State the blood parasite species.
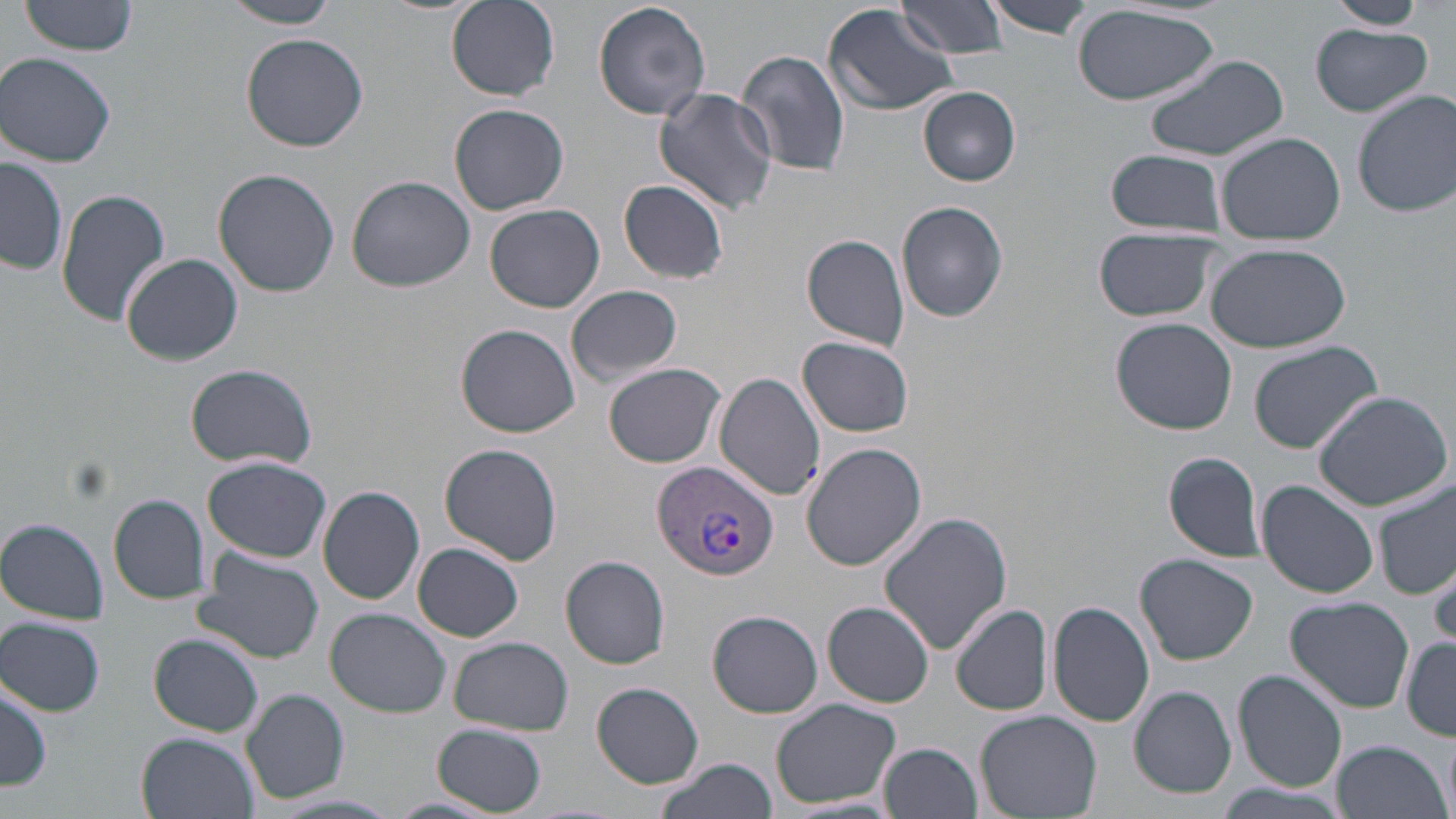

Plasmodium vivax.

Approximate bounding boxes as [x1, y1, x2, y2] in pixels. Plasmodium vivax-infected red blood cell locations: [652, 460, 777, 581]. Uninfected red blood cell locations: [20, 0, 140, 58], [447, 0, 559, 99], [593, 0, 711, 121], [897, 0, 1011, 59], [981, 0, 1097, 40], [1324, 0, 1427, 30], [219, 1, 345, 28], [823, 3, 958, 115], [1070, 6, 1220, 104], [1312, 25, 1433, 118], [241, 32, 368, 152], [737, 49, 851, 180], [1144, 51, 1289, 163], [0, 53, 121, 167], [653, 87, 779, 215], [919, 88, 1020, 185], [1353, 90, 1456, 217], [448, 103, 569, 214], [1216, 131, 1348, 244], [1103, 150, 1229, 239], [1, 157, 69, 277], [214, 170, 339, 298], [347, 176, 474, 292], [619, 178, 729, 284], [56, 188, 170, 327], [896, 201, 1009, 322], [484, 202, 604, 313], [1093, 226, 1225, 323], [801, 235, 912, 350], [1205, 242, 1352, 351], [119, 253, 244, 366], [567, 284, 683, 387], [1111, 319, 1239, 434], [456, 324, 580, 437], [799, 336, 915, 436], [1247, 340, 1383, 454], [184, 362, 318, 469], [604, 362, 726, 468], [714, 372, 826, 501], [1312, 390, 1453, 511], [440, 443, 562, 566], [802, 443, 926, 571], [1163, 450, 1265, 562], [204, 457, 331, 560], [1259, 481, 1379, 601], [1373, 482, 1455, 599], [317, 485, 425, 604], [109, 493, 209, 603], [879, 511, 1013, 657], [1, 516, 110, 624], [413, 544, 523, 643], [193, 550, 326, 664], [1135, 554, 1259, 665], [562, 555, 670, 669], [1425, 559, 1456, 647], [1286, 596, 1413, 713], [822, 601, 934, 707], [1047, 601, 1155, 728], [954, 604, 1054, 715], [706, 608, 824, 719], [326, 609, 455, 716], [1, 618, 104, 716], [149, 634, 263, 737], [449, 636, 572, 736], [1401, 637, 1456, 739], [1234, 670, 1347, 792], [1, 676, 52, 792], [592, 682, 705, 788], [1130, 686, 1235, 799], [243, 688, 350, 804], [769, 698, 902, 810], [975, 708, 1102, 817], [434, 723, 547, 815], [138, 732, 257, 819], [1442, 738, 1455, 819], [1330, 739, 1449, 819], [882, 743, 983, 819], [654, 758, 776, 819], [1217, 783, 1350, 819], [385, 796, 499, 818]. Light microscopy. Image is 1456×819 pixels. May-Grünwald-Giemsa-stained preparation. Thin blood film. One field of a larger specimen. Captured at 1000x magnification.